Give the extent of all uninfected red blood cells.
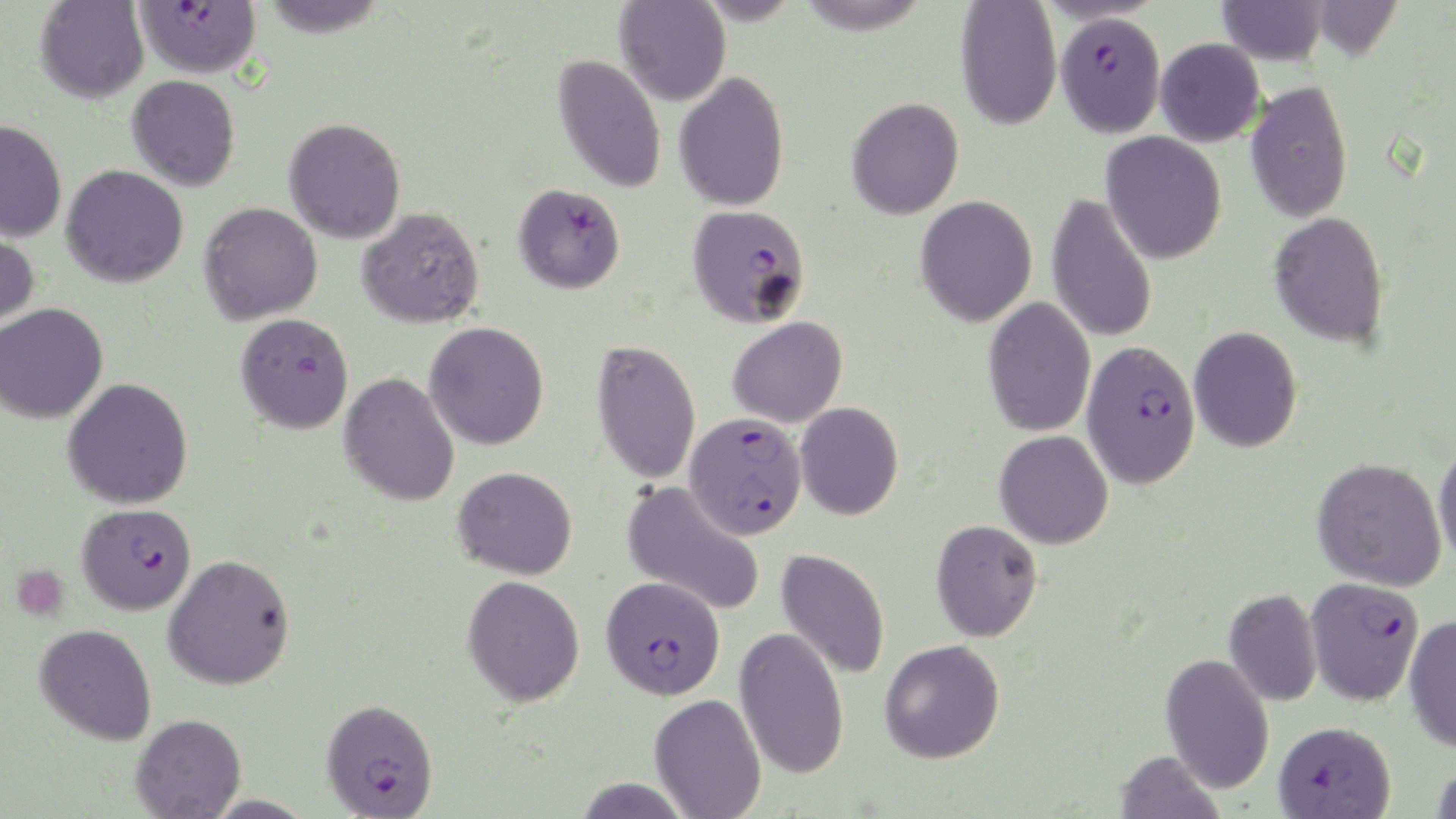

Approximate bounding boxes as (x1, y1, x2, y2) in pixels.
Uninfected red blood cells: (259, 0, 389, 37), (793, 0, 934, 35), (1217, 0, 1328, 65), (1311, 0, 1403, 63), (35, 1, 149, 103), (615, 1, 731, 106), (954, 1, 1062, 131), (1154, 38, 1265, 147), (553, 54, 666, 193), (674, 72, 789, 211), (126, 75, 240, 191), (1245, 79, 1352, 222), (846, 97, 964, 220), (284, 118, 406, 244), (0, 120, 67, 243), (1100, 132, 1227, 264), (61, 165, 188, 288), (1046, 193, 1158, 344), (915, 196, 1038, 327), (199, 202, 322, 325), (356, 207, 484, 329), (1268, 211, 1390, 348), (0, 225, 40, 333), (983, 297, 1096, 438), (0, 303, 108, 423), (236, 312, 354, 434), (727, 316, 848, 427), (424, 321, 549, 450), (1188, 326, 1303, 453), (592, 340, 700, 484), (339, 373, 460, 506), (63, 378, 193, 509), (795, 402, 904, 520), (994, 430, 1113, 549), (1433, 441, 1456, 567), (1312, 457, 1447, 591), (453, 466, 578, 579), (622, 481, 765, 616), (930, 519, 1043, 642), (776, 548, 890, 680), (163, 555, 295, 690), (462, 575, 585, 706), (1223, 588, 1321, 707), (1404, 614, 1456, 751), (34, 623, 157, 745), (735, 626, 849, 780), (879, 639, 1005, 763), (1160, 653, 1275, 794), (649, 694, 766, 819), (130, 714, 246, 819), (1115, 750, 1224, 819), (1428, 766, 1456, 818), (571, 777, 694, 818), (202, 794, 317, 819).

slide-level diagnosis = Plasmodium falciparum
preparation = thin blood film
field of view = one of a larger specimen
image size = 1456×819 pixels
magnification = 1000x
Plasmodium falciparum-infected red blood cell locations = approximate bounding boxes as (x1, y1, x2, y2) in pixels: (135, 1, 261, 79), (1055, 11, 1165, 136), (513, 183, 625, 293), (687, 204, 811, 328), (1081, 340, 1200, 487), (685, 413, 806, 539), (77, 503, 197, 615), (601, 576, 725, 698), (1305, 576, 1425, 704), (321, 698, 438, 818), (1273, 721, 1395, 818)
modality = light microscopy
stain = May-Grünwald-Giemsa
platelet locations = approximate bounding boxes as (x1, y1, x2, y2) in pixels: (12, 566, 68, 623)